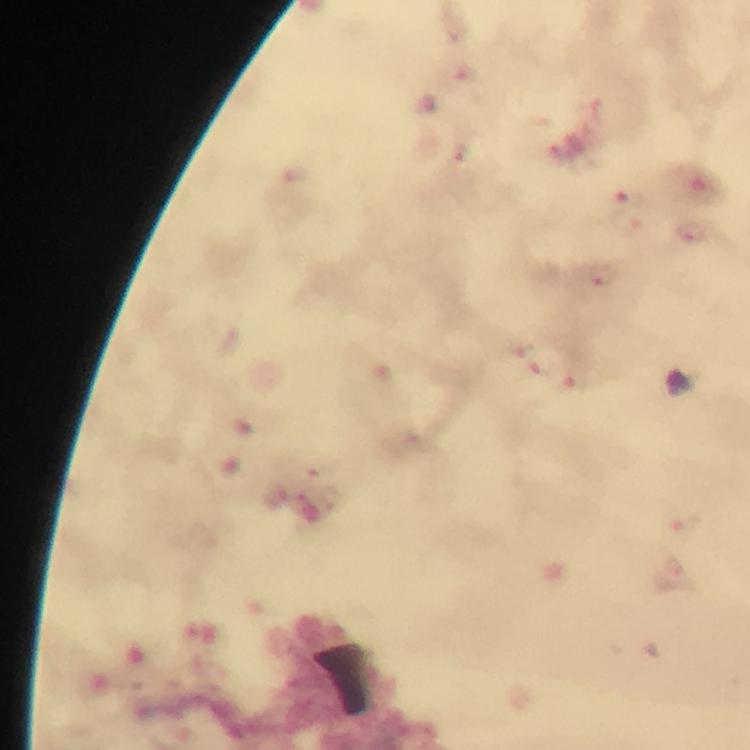

context = from a diagnostic examination for malaria
immersion oil = applied
preparation = thick smear
stain = Giemsa
magnification = 100x
capture = smartphone photograph through a microscope
malaria parasite locations = approximate centers as {x, y} in pixels: {465, 73}, {458, 152}, {629, 198}, {689, 231}, {604, 275}, {520, 347}, {677, 567}
cropped from = one field of view
image size = 750×750 pixels